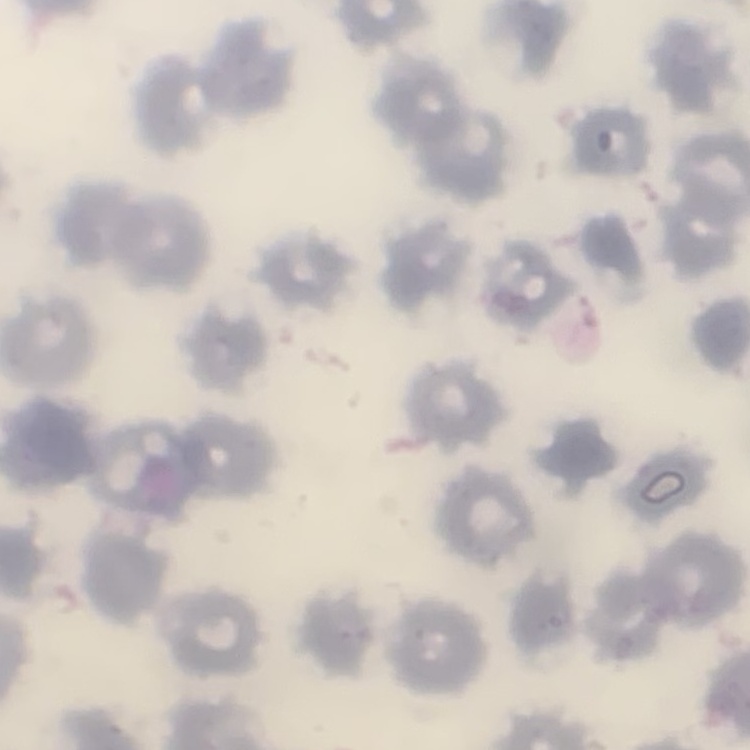

erythrocyte morphology = no rouleaux formation
preparation = thin peripheral smear
stain = Field's or Giemsa
image type = one tile cut from a larger photomicrograph